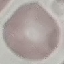
Summary:
  - Result: no malaria parasites seen
  - Stain: Giemsa
  - Preparation: thin blood film
  - Image type: automatically extracted cell patch, resized to 64 × 64 pixels
  - Capture: smartphone through the microscope eyepiece